Classify this cell by malaria status.
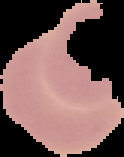

Uninfected.

The area outside the segmented cell region is set to black. Image is 124×157 pixels. From a thin blood film.